Locate every blood parasite and identify its species.
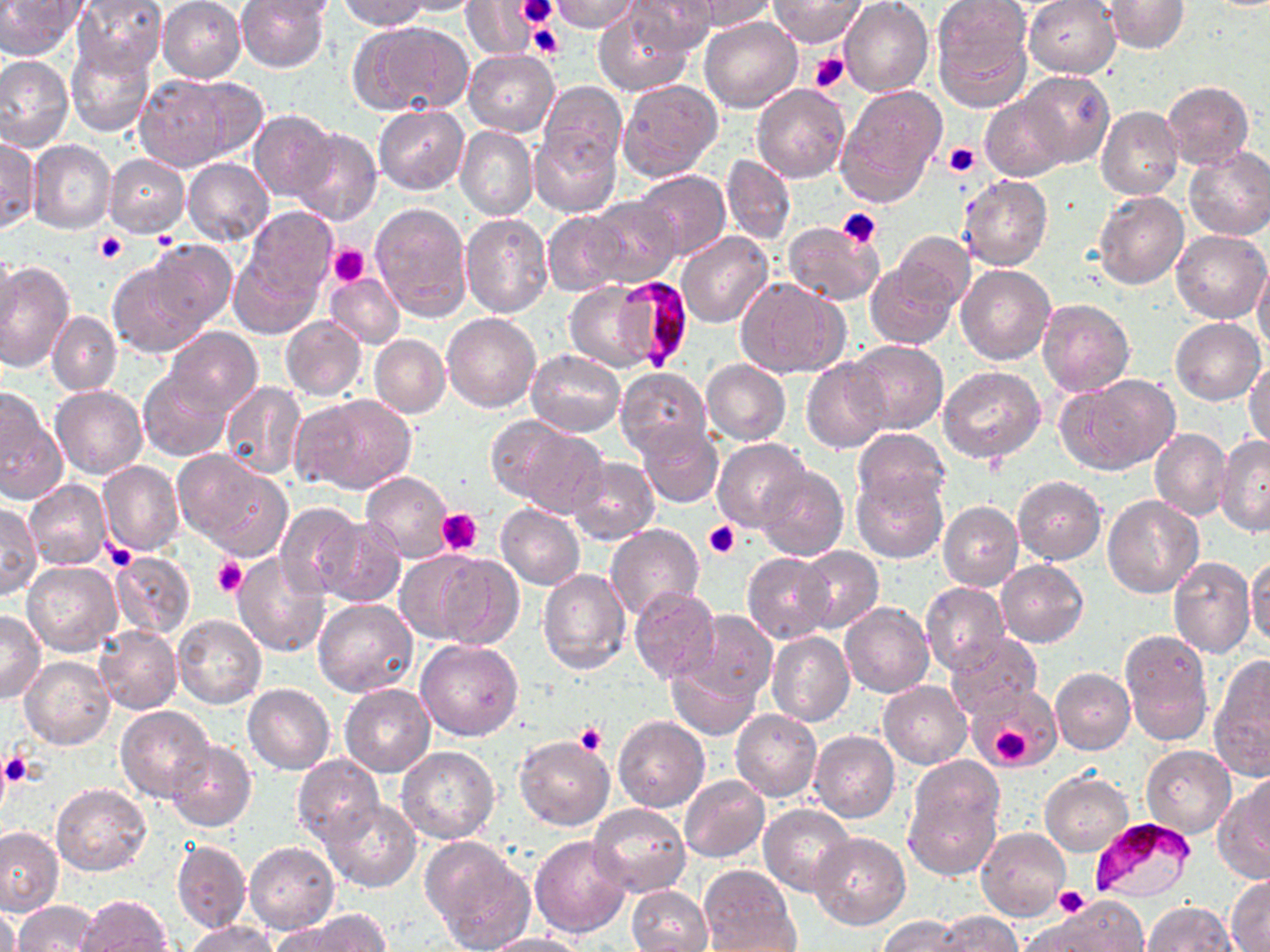

Approximate bounding boxes as (x1,y1)-(x2,y2) corner pairs in pixels.
Plasmodium falciparum-infected red blood cells: (612,276)-(693,369), (1089,817)-(1198,903).
No Plasmodium ovale, Plasmodium malariae, Plasmodium vivax, Babesia divergens, or Trypanosoma brucei observed.

Summary:
  - Uninfected red blood cell locations: (0,0)-(80,60), (72,0)-(166,78), (235,0)-(329,72), (248,0)-(339,21), (340,0)-(428,31), (394,0)-(486,15), (551,0)-(642,34), (624,0)-(719,55), (680,0)-(775,32), (769,0)-(865,48), (930,0)-(1034,110), (1024,0)-(1121,78), (1103,0)-(1189,53), (158,1)-(246,83), (840,1)-(933,97), (459,2)-(539,59), (594,9)-(692,98), (699,17)-(802,113), (353,20)-(474,116), (66,38)-(154,138), (464,49)-(560,135), (0,54)-(75,154), (1019,71)-(1115,168), (134,75)-(233,171), (179,77)-(269,162), (617,79)-(723,182), (1161,81)-(1254,170), (539,82)-(627,168), (751,83)-(849,181), (835,85)-(946,206), (980,95)-(1070,181), (373,105)-(469,193), (1097,106)-(1183,202), (248,108)-(340,203), (455,124)-(537,221), (530,127)-(621,216), (291,129)-(382,225), (0,136)-(38,233), (28,140)-(116,234), (1184,146)-(1270,241), (721,153)-(796,247), (105,154)-(189,236), (183,157)-(274,246), (632,170)-(731,259), (958,173)-(1053,272), (1093,193)-(1189,290), (584,197)-(682,287), (370,202)-(472,319), (241,207)-(338,300), (543,211)-(627,295), (461,213)-(552,318), (783,221)-(883,305), (1173,229)-(1269,322), (887,231)-(977,319), (676,232)-(771,328), (145,240)-(238,331), (227,247)-(322,340), (0,249)-(20,343), (0,259)-(74,372), (865,259)-(960,349), (107,260)-(209,357), (956,263)-(1055,365), (1253,264)-(1270,353), (325,274)-(405,349), (734,276)-(848,379), (564,281)-(663,373), (1037,297)-(1134,396), (442,311)-(542,412), (47,312)-(121,395), (280,315)-(366,400), (1170,317)-(1265,405), (165,326)-(262,417), (369,335)-(449,418), (849,340)-(947,433), (528,348)-(624,436), (1246,357)-(1270,451), (801,358)-(891,454), (702,359)-(791,445), (939,367)-(1046,464), (615,368)-(711,458), (138,370)-(231,461), (1059,374)-(1180,475), (221,382)-(307,480), (51,386)-(146,479), (293,393)-(417,495), (1,397)-(66,506), (493,418)-(607,517), (636,423)-(723,508), (851,426)-(951,514), (1150,428)-(1231,520), (1215,435)-(1270,538), (711,438)-(812,533), (175,450)-(290,559), (567,457)-(659,544), (98,461)-(184,556), (754,465)-(848,561), (850,469)-(947,564), (361,470)-(455,561), (1012,476)-(1106,564), (24,479)-(111,570), (1101,495)-(1203,597), (938,500)-(1023,591), (275,503)-(364,599), (496,503)-(584,589), (0,504)-(41,598), (312,516)-(406,607), (605,525)-(705,621), (798,545)-(883,633), (397,550)-(502,645), (110,551)-(195,639), (231,551)-(332,658), (741,552)-(835,643), (1247,555)-(1270,646), (1168,558)-(1255,659), (997,560)-(1088,647), (23,562)-(121,656), (537,569)-(630,675), (920,583)-(1010,675), (628,587)-(721,684), (312,598)-(419,697), (840,602)-(933,698), (0,610)-(45,704), (677,610)-(776,707), (171,614)-(266,709), (93,626)-(183,715), (1119,629)-(1213,746), (768,631)-(855,726), (945,633)-(1041,717), (416,639)-(524,740), (665,650)-(763,740), (21,657)-(115,751), (1209,658)-(1270,779), (1051,667)-(1135,756), (879,681)-(971,769), (244,682)-(335,773), (340,684)-(435,777), (117,705)-(213,800), (730,709)-(821,801), (613,717)-(710,814), (517,727)-(707,819), (810,730)-(900,822), (515,735)-(615,831), (165,740)-(256,833), (1141,745)-(1237,837), (397,747)-(499,844), (292,755)-(384,849), (904,758)-(1003,874), (1246,769)-(1270,859), (1041,772)-(1132,856), (680,774)-(770,862), (1214,784)-(1270,883), (51,785)-(151,876), (323,798)-(423,893), (589,803)-(690,899), (759,804)-(856,897), (0,827)-(63,915), (977,828)-(1069,922), (810,833)-(910,930), (530,834)-(631,936), (421,838)-(535,952), (172,840)-(251,932), (245,841)-(340,933), (700,866)-(800,949), (1226,876)-(1270,951), (626,884)-(712,952), (74,894)-(172,952), (1041,897)-(1149,952), (12,901)-(103,951), (1142,902)-(1238,951), (0,905)-(20,952), (298,909)-(392,951), (933,910)-(1025,951), (876,916)-(972,951), (187,920)-(280,952), (482,933)-(590,952)
  - Platelet locations: (519,0)-(556,25), (523,8)-(559,51), (528,26)-(564,60), (810,52)-(850,94), (944,142)-(980,177), (838,206)-(883,249), (93,233)-(127,264), (331,245)-(369,287), (436,508)-(481,555), (704,521)-(739,559), (103,542)-(135,571), (213,556)-(246,596), (986,720)-(1034,769), (574,723)-(607,756), (1,748)-(36,788), (1054,885)-(1089,918)
  - Slide-level diagnosis: Plasmodium falciparum
  - Field of view: one of a larger specimen
  - Modality: light microscopy
  - Magnification: 1000x
  - Preparation: thin blood smear
  - Stain: May-Grünwald-Giemsa
  - Image size: 1270×952 pixels